Assess the morphology of the red blood cells.
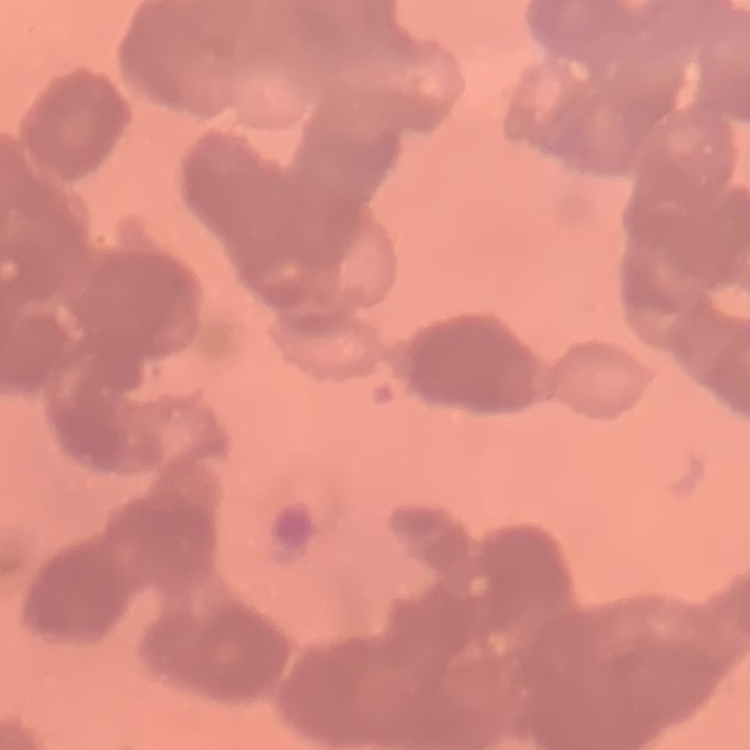

They show rouleaux formation.

{
  "stain": "Field's or Giemsa",
  "preparation": "thin blood smear",
  "image_type": "square crop of a larger photomicrograph"
}